Identify the preparation type.
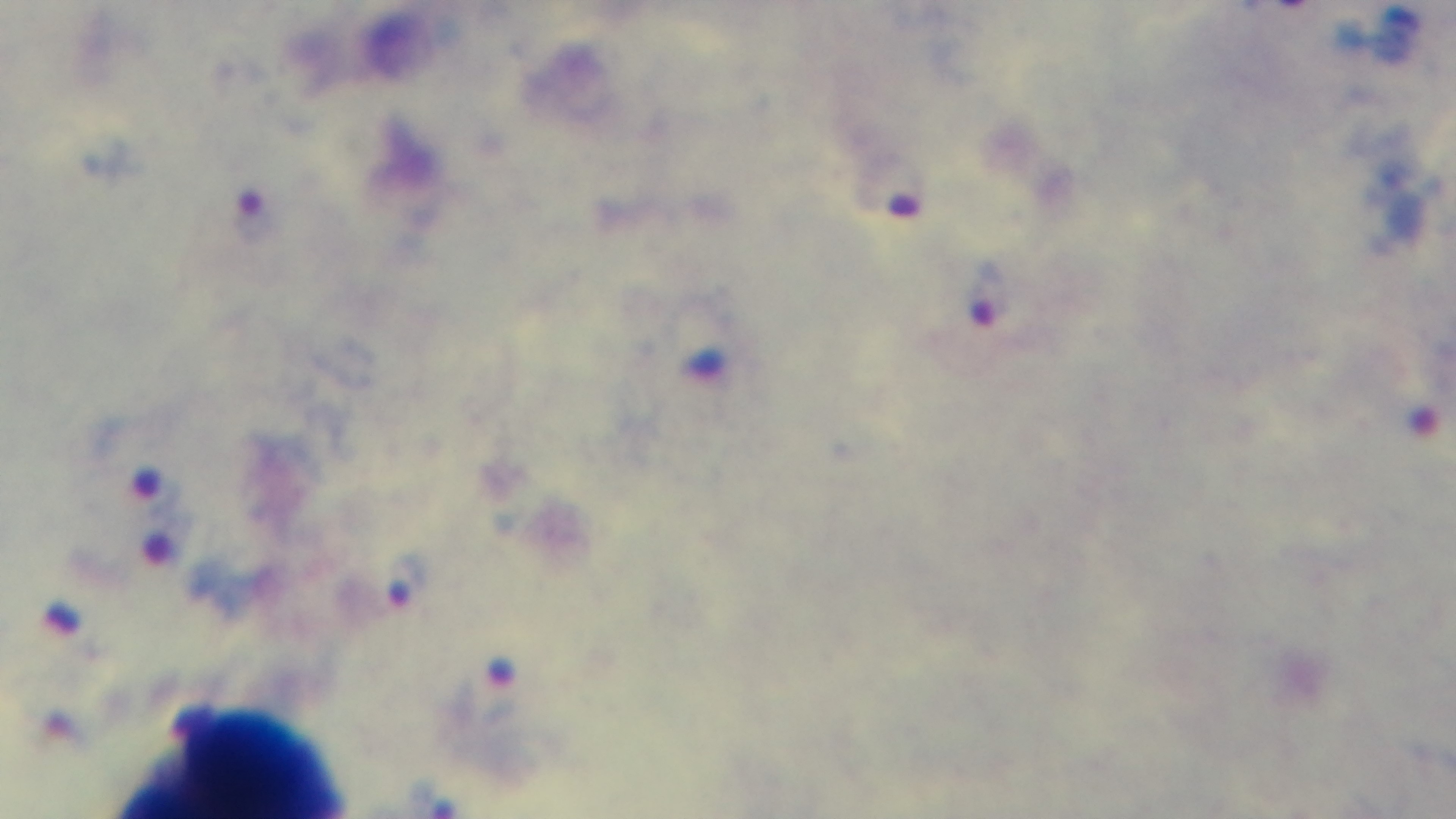
A thick smear.

stain = Giemsa
malaria status = positive
capture = mounted 4K digital camera
objective = 100x oil immersion
field of view = single
modality = light microscopy